Report the malaria status of this cell.
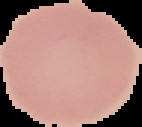
Uninfected.

From a thin blood smear. Image is 142×127 pixels. Cell region segmented out of the field of view; the surrounding area is masked to black.